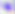

Micrograph. 400x magnification. Toxoplasma gondii is seen.